Describe the morphology of the erythrocytes.
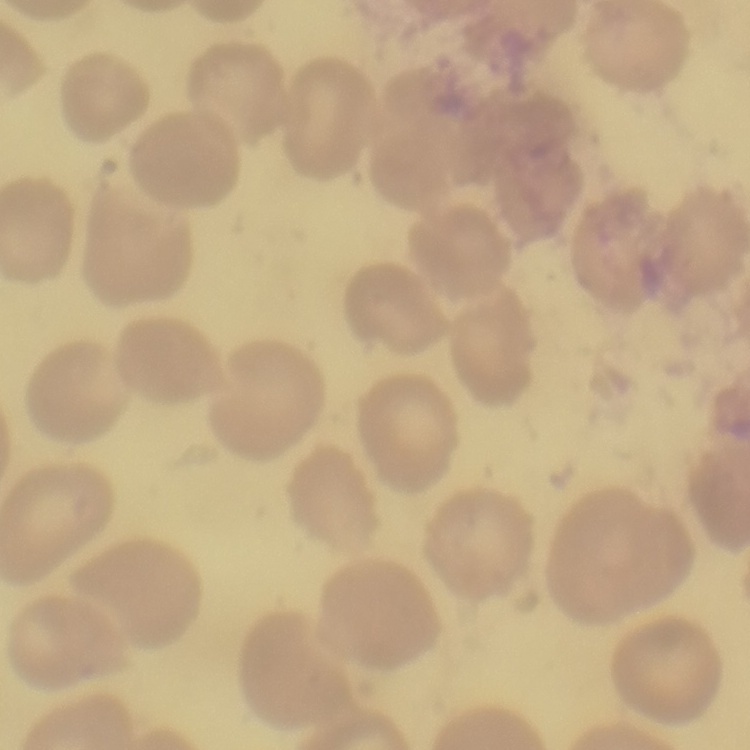

No rouleaux formation.

stain = Field's or Giemsa
preparation = thin peripheral smear
image type = square crop of a larger photomicrograph